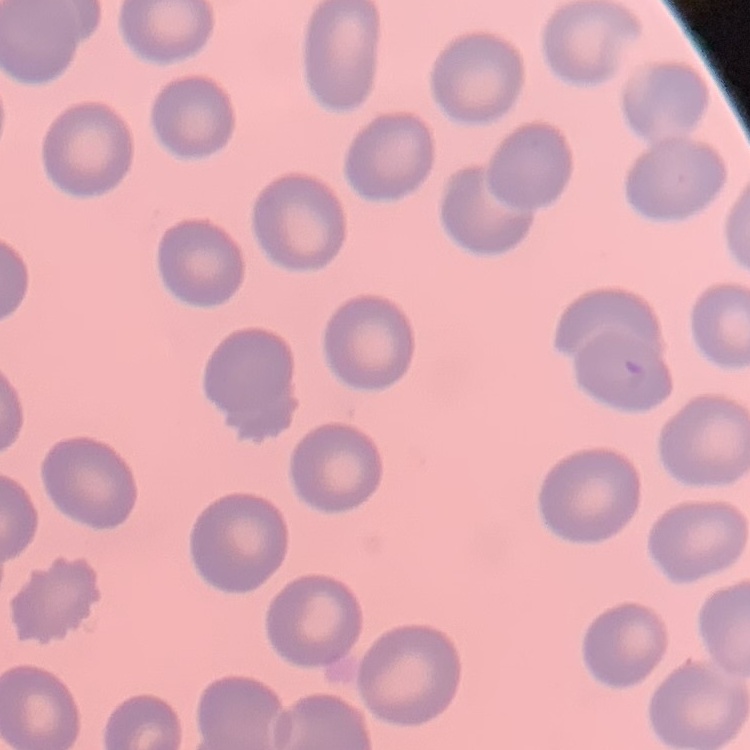
The erythrocytes show no rouleaux formation. Thin blood smear. Stained with either Field's or Giemsa. One tile cut from a larger photomicrograph.